Comment on the morphology of the red blood cells.
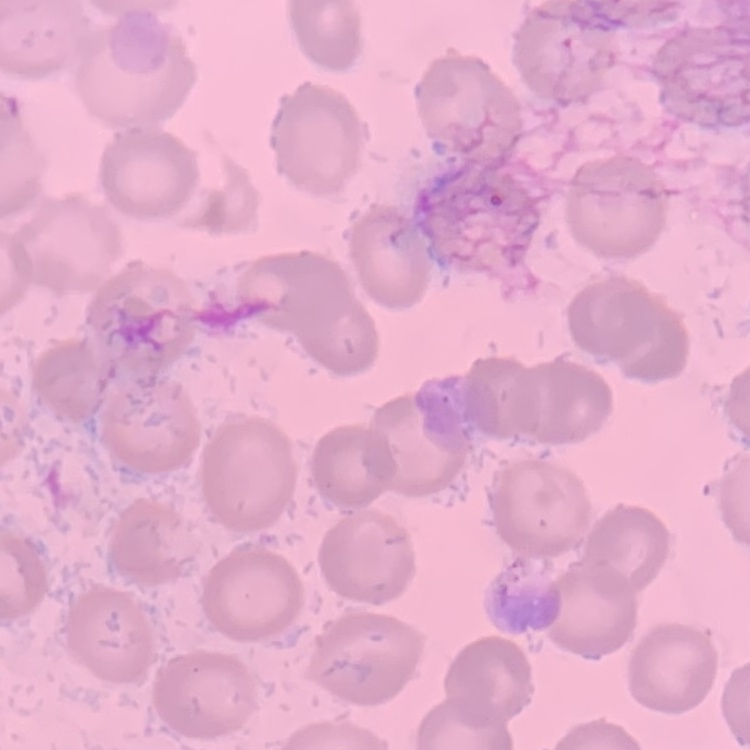
No rouleaux formation.

Field's or Giemsa stain. One tile cut from a larger photomicrograph. Thin blood smear.